Locate every blood parasite and identify its species.
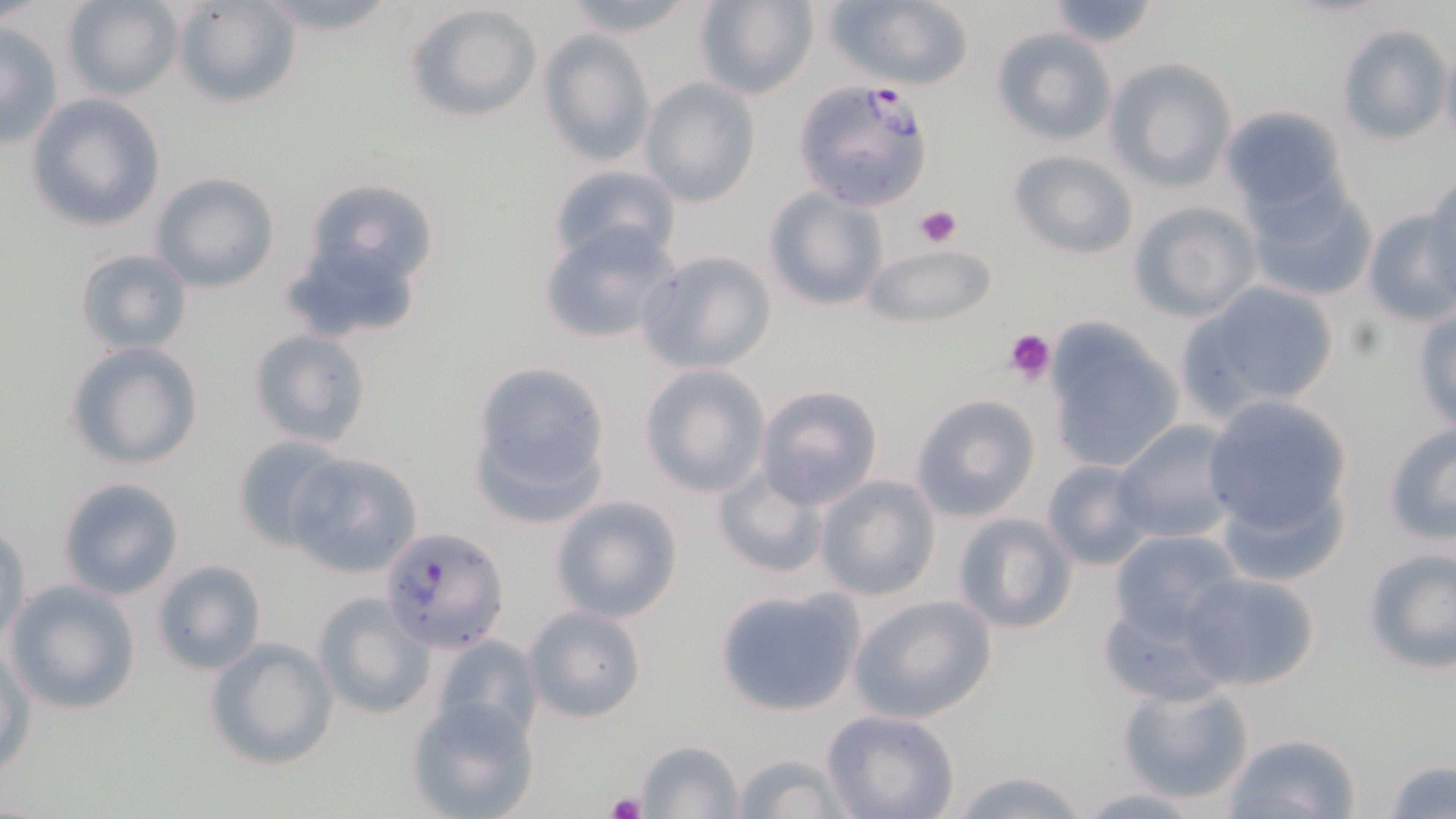
Approximate bounding boxes as (x1, y1, x2, y2) in pixels.
Plasmodium falciparum-infected red blood cells: (804, 79, 940, 208), (380, 526, 507, 652).
No Plasmodium ovale, Plasmodium malariae, Plasmodium vivax, Babesia divergens, or Trypanosoma brucei observed.

Platelet locations: (915, 203, 962, 248), (1004, 329, 1056, 381), (608, 791, 646, 819). Uninfected red blood cell locations: (63, 0, 181, 101), (249, 0, 405, 36), (556, 0, 703, 38), (693, 0, 818, 100), (823, 0, 975, 91), (172, 1, 300, 108), (1043, 1, 1166, 50), (406, 3, 543, 122), (1335, 23, 1451, 145), (0, 24, 63, 150), (989, 27, 1119, 147), (538, 31, 654, 167), (1441, 40, 1456, 154), (1105, 58, 1237, 192), (639, 77, 761, 207), (26, 93, 167, 233), (1219, 105, 1350, 218), (1009, 148, 1138, 259), (545, 162, 680, 273), (150, 172, 281, 293), (289, 177, 442, 320), (1243, 178, 1378, 303), (1424, 178, 1456, 288), (763, 187, 889, 312), (1128, 199, 1261, 323), (1361, 205, 1454, 328), (536, 222, 680, 345), (862, 245, 995, 329), (74, 247, 193, 355), (639, 250, 777, 375), (1174, 281, 1340, 423), (1412, 304, 1456, 436), (1043, 322, 1184, 474), (248, 328, 374, 450), (63, 341, 206, 470), (466, 358, 616, 525), (639, 363, 771, 498), (755, 384, 884, 509), (909, 394, 1041, 522), (1201, 395, 1353, 540), (1113, 419, 1243, 543), (1380, 423, 1456, 547), (229, 438, 349, 552), (283, 452, 422, 577), (1041, 458, 1157, 571), (711, 464, 828, 581), (815, 475, 941, 600), (56, 476, 184, 601), (1215, 480, 1351, 587), (550, 494, 684, 623), (950, 512, 1079, 635), (0, 519, 30, 646), (1107, 529, 1244, 642), (1359, 546, 1455, 674), (151, 559, 269, 677), (1183, 571, 1321, 691), (5, 580, 142, 715), (713, 586, 865, 716), (313, 592, 434, 720), (846, 594, 997, 724), (1099, 594, 1232, 704), (524, 605, 649, 723), (431, 633, 542, 744), (205, 636, 340, 771), (1, 647, 35, 776), (1116, 682, 1255, 806), (404, 696, 541, 819), (822, 710, 960, 819), (1222, 731, 1362, 818), (633, 738, 745, 818), (722, 751, 856, 818), (1383, 757, 1456, 819), (945, 767, 1097, 819), (1069, 784, 1222, 818). Slide-level diagnosis: Plasmodium falciparum. One field of a larger specimen. Light microscopy. Image is 1456×819 pixels. Thin blood film. May-Grünwald-Giemsa stain. 1000x magnification.